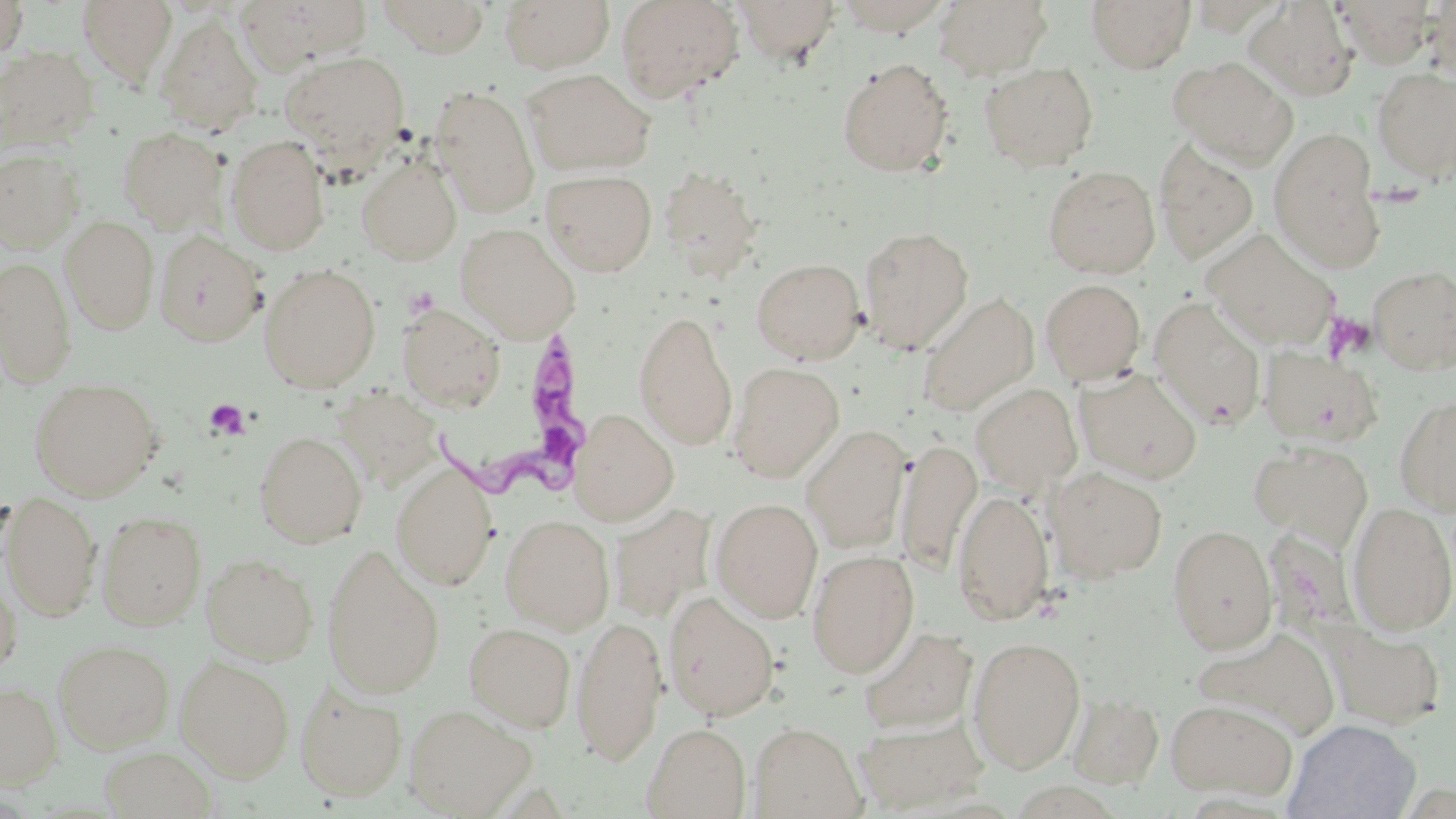

slide-level diagnosis = Trypanosoma brucei
modality = light microscopy
preparation = thin blood smear
magnification = 1000x
image size = 1456×819 pixels
stain = May-Grünwald-Giemsa
field of view = one of a larger specimen
platelet locations = approximate bounding boxes as [x1, y1, x2, y2] in pixels: [402, 285, 439, 320], [1323, 312, 1376, 362], [204, 399, 249, 440]
Trypanosoma brucei locations = approximate bounding boxes as [x1, y1, x2, y2] in pixels: [438, 324, 601, 504]
uninfected red blood cell locations = approximate bounding boxes as [x1, y1, x2, y2] in pixels: [0, 0, 29, 61], [236, 0, 374, 71], [377, 0, 491, 57], [499, 0, 615, 72], [616, 0, 743, 103], [732, 0, 841, 66], [831, 0, 954, 35], [933, 0, 1053, 80], [1086, 0, 1196, 73], [1332, 0, 1437, 68], [78, 1, 177, 88], [1242, 2, 1357, 101], [155, 14, 263, 137], [0, 46, 100, 150], [280, 51, 409, 160], [1168, 55, 1298, 168], [838, 58, 954, 176], [979, 61, 1099, 172], [522, 68, 656, 176], [1372, 68, 1456, 181], [430, 85, 540, 217], [117, 126, 229, 234], [1268, 128, 1385, 272], [225, 134, 331, 254], [1154, 138, 1259, 265], [0, 149, 83, 251], [356, 157, 462, 265], [659, 164, 764, 281], [1043, 165, 1160, 278], [540, 169, 657, 276], [61, 216, 160, 335], [455, 223, 580, 342], [858, 226, 973, 354], [1203, 228, 1340, 351], [153, 230, 266, 346], [1, 257, 77, 387], [751, 257, 866, 364], [260, 263, 381, 392], [1369, 265, 1456, 373], [1041, 278, 1146, 384], [918, 293, 1039, 417], [1148, 296, 1266, 429], [397, 303, 505, 412], [634, 309, 738, 450], [1258, 345, 1384, 447], [729, 361, 844, 482], [1074, 367, 1203, 484], [30, 378, 162, 501], [335, 381, 438, 493], [971, 383, 1082, 493], [1395, 395, 1456, 517], [570, 409, 678, 526], [802, 424, 911, 554], [255, 431, 367, 548], [896, 438, 981, 573], [1249, 440, 1373, 550], [390, 461, 499, 590], [1048, 466, 1168, 583], [952, 488, 1054, 625], [1, 493, 102, 621], [710, 497, 824, 623], [1347, 502, 1456, 635], [609, 504, 716, 623], [97, 510, 207, 629], [499, 514, 615, 634], [1167, 524, 1277, 654], [321, 545, 445, 699], [806, 549, 919, 678], [202, 553, 319, 665], [0, 569, 21, 677], [663, 591, 780, 721], [571, 613, 668, 766], [464, 621, 577, 731], [1320, 621, 1446, 729], [859, 627, 978, 735], [1191, 628, 1343, 744], [967, 636, 1085, 773], [53, 639, 174, 753], [175, 655, 295, 781], [0, 682, 62, 787], [295, 682, 407, 801], [1068, 694, 1163, 789], [1165, 698, 1298, 802], [404, 704, 536, 818], [853, 713, 989, 814], [1284, 718, 1420, 819], [749, 721, 864, 818], [643, 722, 751, 818], [101, 745, 217, 819]